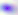
magnification = 400x
modality = photomicrograph
identification = Toxoplasma gondii